Locate every blood parasite and identify its species.
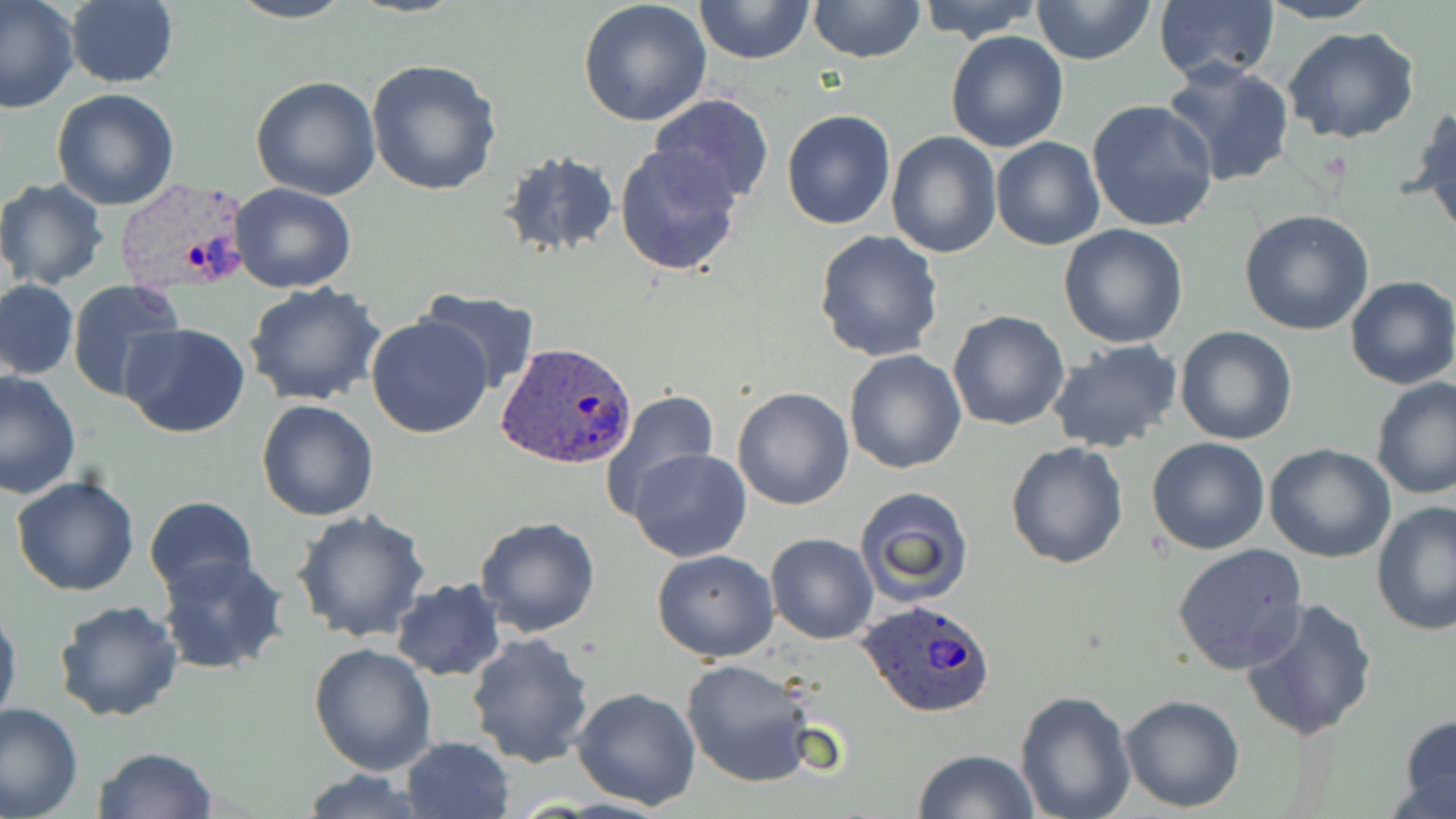
Approximate bounding boxes as (x1,y1)-(x2,y2) corner pairs in pixels.
Plasmodium ovale-infected red blood cells: (112,177)-(256,296), (496,341)-(637,467), (859,598)-(998,717).
No Plasmodium falciparum, Plasmodium malariae, Plasmodium vivax, Babesia divergens, or Trypanosoma brucei observed.

slide-level diagnosis = Plasmodium ovale
preparation = thin blood smear
modality = light microscopy
uninfected red blood cell locations = approximate bounding boxes as (x1,y1)-(x2,y2) corner pairs in pixels: (227,0)-(354,24), (695,0)-(814,66), (808,0)-(925,65), (917,0)-(1041,41), (1032,0)-(1154,65), (1256,0)-(1384,25), (0,1)-(79,113), (578,1)-(713,127), (63,2)-(179,87), (1153,2)-(1280,86), (1281,27)-(1423,145), (944,30)-(1070,152), (365,57)-(502,197), (1160,61)-(1295,189), (250,76)-(382,201), (52,88)-(180,210), (649,92)-(774,205), (1086,99)-(1219,233), (1409,105)-(1456,238), (781,108)-(896,230), (885,130)-(1002,258), (991,136)-(1106,252), (614,143)-(745,279), (496,149)-(621,263), (0,179)-(111,290), (230,183)-(359,294), (1239,209)-(1375,336), (1058,225)-(1189,349), (814,229)-(945,362), (1345,276)-(1456,389), (1,280)-(78,381), (65,281)-(188,403), (244,281)-(384,407), (416,289)-(542,395), (947,309)-(1070,431), (366,315)-(493,440), (120,322)-(253,439), (1174,326)-(1298,445), (1162,330)-(1282,555), (1046,340)-(1184,454), (843,349)-(967,475), (0,370)-(81,500), (1370,376)-(1456,499), (732,387)-(854,511), (599,388)-(718,513), (256,399)-(380,521), (1147,437)-(1270,554), (1005,442)-(1129,569), (1264,442)-(1396,563), (628,448)-(751,562), (10,474)-(141,596), (856,484)-(977,610), (144,496)-(258,601), (1371,500)-(1456,633), (292,507)-(431,644), (475,517)-(602,638), (765,533)-(878,645), (1172,543)-(1308,673), (651,548)-(780,662), (157,554)-(291,676), (390,578)-(506,680), (1241,597)-(1378,741), (53,599)-(184,721), (0,600)-(21,733), (466,632)-(595,769), (309,644)-(437,776), (680,658)-(820,789), (572,685)-(702,810), (1014,689)-(1137,819), (1119,693)-(1246,811), (0,701)-(83,819), (1397,712)-(1455,818), (402,736)-(515,819), (94,745)-(219,819), (914,746)-(1039,818), (299,768)-(431,818)
image size = 1456×819 pixels
stain = May-Grünwald-Giemsa
magnification = 1000x
field of view = one of a larger specimen